Locate and identify every blood parasite.
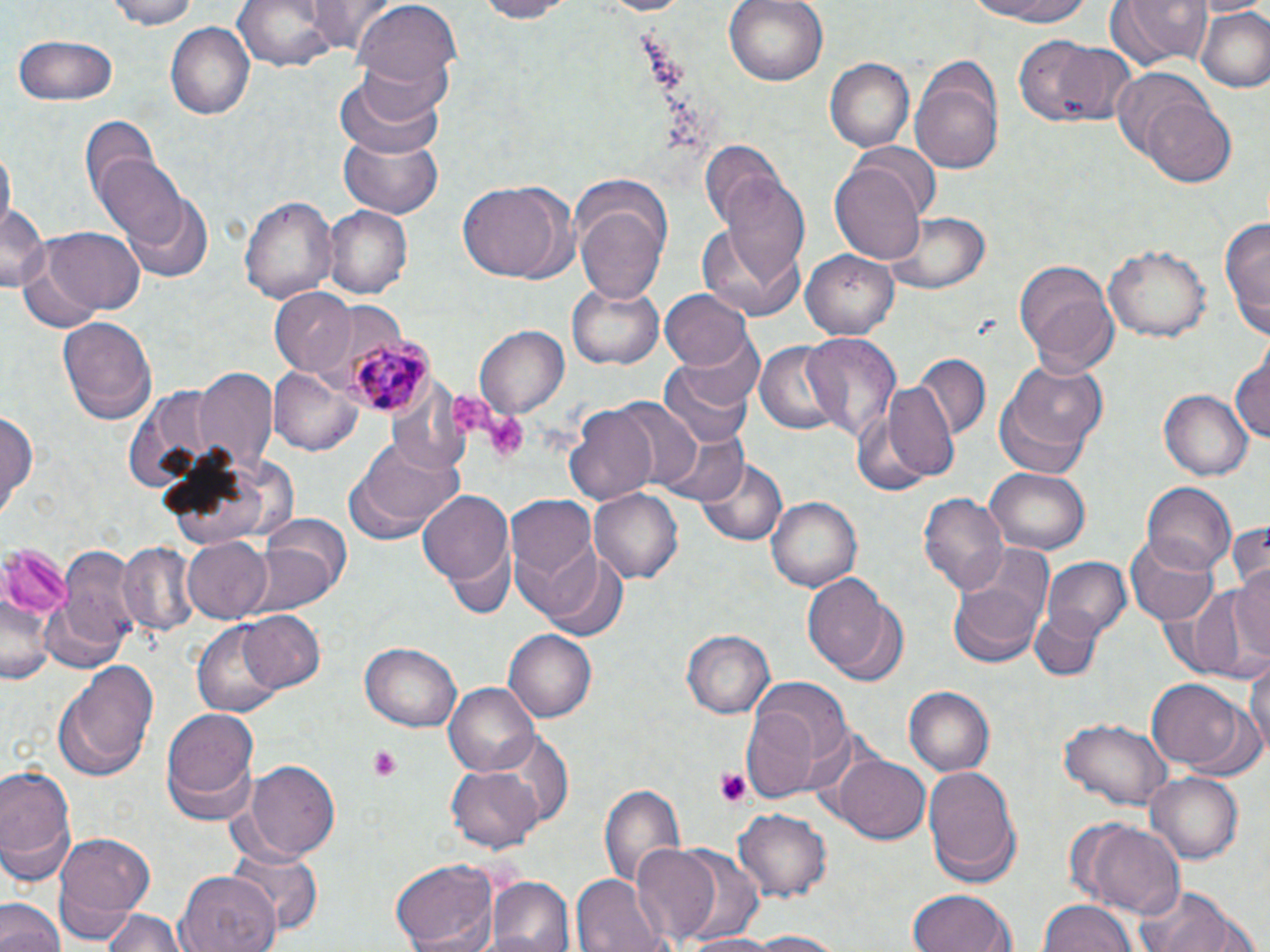
Approximate bounding boxes as (x1,y1)-(x2,y2) corner pairs in pixels.
Plasmodium malariae-infected red blood cells: (345,333)-(434,416).
No Plasmodium falciparum, Plasmodium ovale, Plasmodium vivax, Babesia divergens, or Trypanosoma brucei observed.

Platelet locations: (452,393)-(492,435), (485,411)-(529,464), (366,744)-(404,781), (715,768)-(752,807). Uninfected red blood cell locations: (97,0)-(208,28), (309,0)-(398,53), (470,0)-(572,22), (587,0)-(691,15), (723,0)-(831,87), (954,0)-(1103,25), (1107,0)-(1213,69), (235,2)-(345,74), (355,2)-(460,97), (1196,8)-(1270,93), (167,23)-(255,119), (14,35)-(118,106), (1015,37)-(1139,132), (911,56)-(1007,174), (826,57)-(914,153), (337,63)-(447,157), (1112,70)-(1217,166), (1135,99)-(1237,187), (82,113)-(159,207), (338,133)-(443,219), (2,142)-(15,232), (697,143)-(786,230), (851,143)-(939,224), (93,152)-(188,248), (832,163)-(928,265), (715,168)-(812,290), (457,179)-(567,283), (573,184)-(672,303), (120,187)-(214,281), (238,194)-(336,304), (0,202)-(46,291), (323,206)-(413,298), (884,209)-(991,295), (1219,214)-(1270,338), (697,221)-(806,323), (28,226)-(148,322), (1104,242)-(1210,344), (801,250)-(898,337), (1014,261)-(1119,375), (566,284)-(666,370), (269,289)-(355,376), (660,290)-(755,372), (57,314)-(155,422), (475,325)-(570,419), (675,325)-(766,418), (799,332)-(902,444), (754,342)-(845,437), (1232,349)-(1270,444), (913,352)-(989,440), (998,358)-(1107,468), (660,359)-(756,452), (271,365)-(361,457), (194,370)-(276,476), (866,383)-(960,488), (1160,388)-(1254,480), (596,395)-(706,493), (564,404)-(660,507), (0,407)-(39,519), (660,428)-(748,506), (353,435)-(464,535), (695,457)-(787,547), (986,466)-(1091,554), (1141,482)-(1235,575), (418,487)-(514,597), (590,490)-(685,582), (918,492)-(1009,598), (504,494)-(598,598), (767,498)-(861,591), (255,511)-(351,604), (1224,519)-(1270,595), (1123,534)-(1219,626), (181,538)-(274,623), (116,543)-(199,637), (56,547)-(145,653), (541,550)-(627,640), (1043,555)-(1131,640), (1230,559)-(1270,668), (803,573)-(899,678), (947,580)-(1045,669), (1180,582)-(1270,679), (1029,607)-(1103,682), (237,608)-(325,694), (194,624)-(285,720), (503,629)-(596,723), (683,630)-(774,719), (361,640)-(464,732), (1246,652)-(1270,760), (54,658)-(157,781), (1148,679)-(1247,767), (444,681)-(539,776), (742,686)-(842,803), (903,686)-(994,776), (160,708)-(261,823), (1059,716)-(1173,810), (832,753)-(931,846), (244,759)-(341,861), (924,762)-(1022,886), (0,763)-(78,880), (446,765)-(544,852), (1148,772)-(1244,861), (599,781)-(686,895), (733,809)-(832,901), (1081,821)-(1188,919), (51,832)-(153,935), (628,844)-(726,949), (224,849)-(324,941), (390,860)-(501,952), (177,871)-(278,952), (569,873)-(668,952), (486,875)-(574,952), (1133,885)-(1251,952), (908,888)-(1016,952), (0,897)-(64,952), (1040,898)-(1136,952), (97,909)-(187,952), (738,930)-(850,951), (682,932)-(777,952). Slide-level diagnosis: Plasmodium malariae. Light microscopy. Image is 1270×952 pixels. One field of a larger specimen. May-Grünwald-Giemsa stain. Thin blood smear. 1000x magnification.